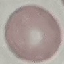

malaria status = uninfected
image type = automatically extracted cell patch, resized to 64 × 64 pixels
stain = Giemsa
preparation = thin blood smear
capture = smartphone camera at the microscope eyepiece